Locate and identify every blood parasite.
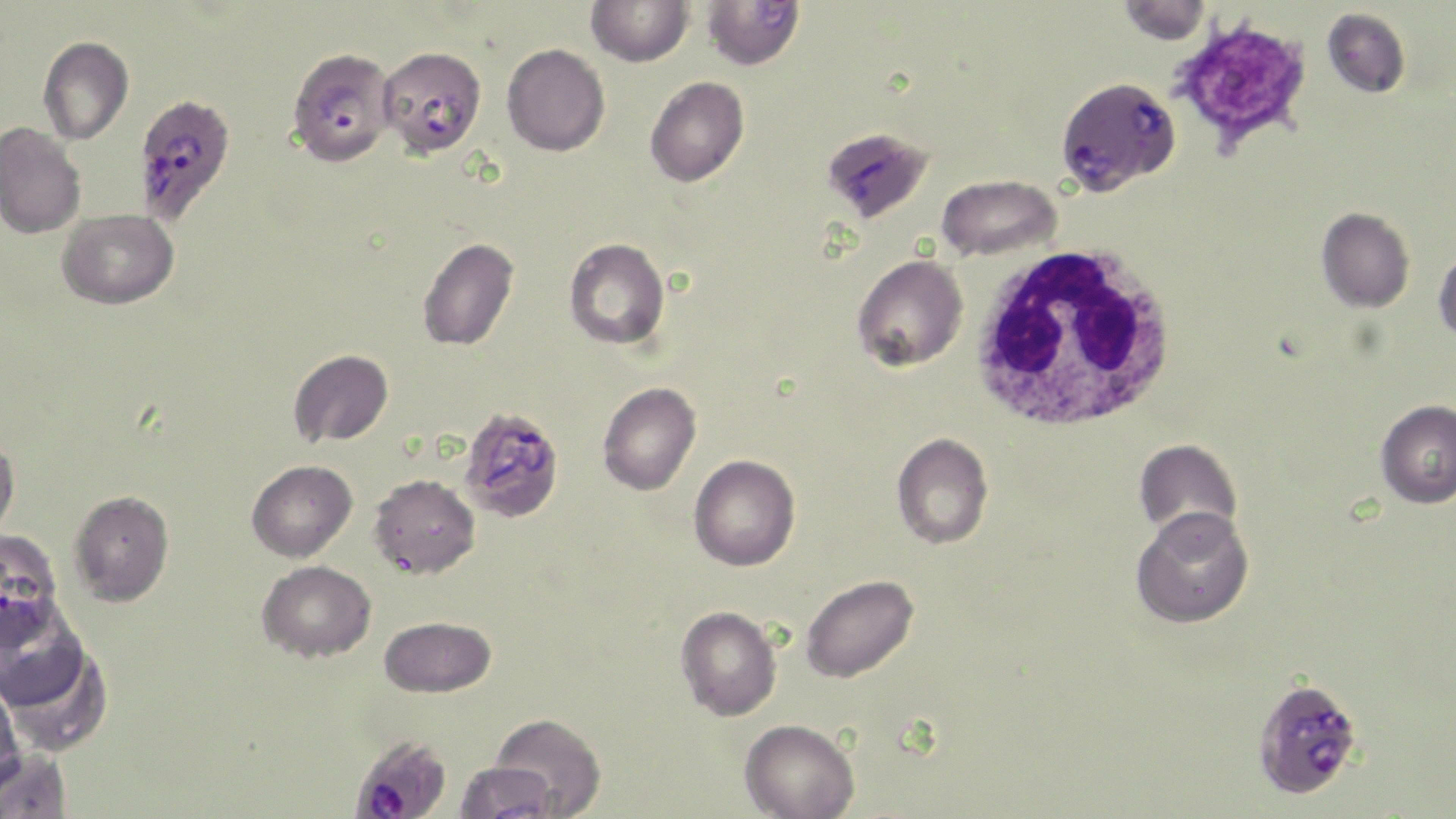
Approximate bounding boxes as [x1, y1, x2, y2] in pixels.
Plasmodium falciparum-infected red blood cells: [290, 50, 398, 170], [385, 52, 487, 153], [1055, 76, 1180, 195], [139, 101, 228, 222], [822, 127, 934, 224], [462, 412, 564, 519], [0, 528, 63, 637], [1250, 677, 1363, 801], [350, 734, 453, 819].
No Plasmodium ovale, Plasmodium malariae, Plasmodium vivax, Babesia divergens, or Trypanosoma brucei observed.

White blood cell locations: [968, 245, 1178, 433]. Platelet locations: [1170, 15, 1314, 156]. Uninfected red blood cell locations: [586, 0, 693, 67], [701, 0, 806, 72], [1117, 0, 1211, 45], [1322, 8, 1410, 98], [38, 36, 134, 144], [502, 43, 610, 156], [644, 77, 749, 187], [0, 122, 86, 239], [937, 174, 1062, 261], [1316, 207, 1414, 313], [57, 209, 179, 309], [417, 237, 519, 351], [564, 238, 670, 350], [1433, 247, 1456, 344], [851, 254, 968, 372], [288, 350, 393, 447], [597, 382, 702, 495], [1375, 399, 1456, 508], [891, 432, 994, 550], [0, 434, 20, 540], [1134, 438, 1242, 540], [689, 454, 800, 571], [246, 460, 357, 561], [368, 473, 480, 579], [70, 490, 174, 606], [1130, 507, 1254, 628], [258, 560, 376, 662], [800, 574, 919, 683], [0, 591, 90, 711], [675, 605, 782, 721], [379, 616, 496, 697], [3, 640, 113, 757], [0, 680, 23, 794], [490, 713, 606, 817], [739, 718, 860, 819], [0, 747, 71, 818], [454, 761, 557, 818]. Slide-level diagnosis: Plasmodium falciparum. Thin blood smear. Optical microscopy. Image is 1456×819 pixels. May-Grünwald-Giemsa stain. 1000x magnification. Single field of view.